Report the malaria status of this cell.
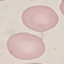

Uninfected.

Thin blood film. Giemsa-stained preparation. Automatically extracted cell patch, resized to 64 × 64 pixels. Acquired by smartphone through the microscope eyepiece.